Comment on the morphology of the erythrocytes.
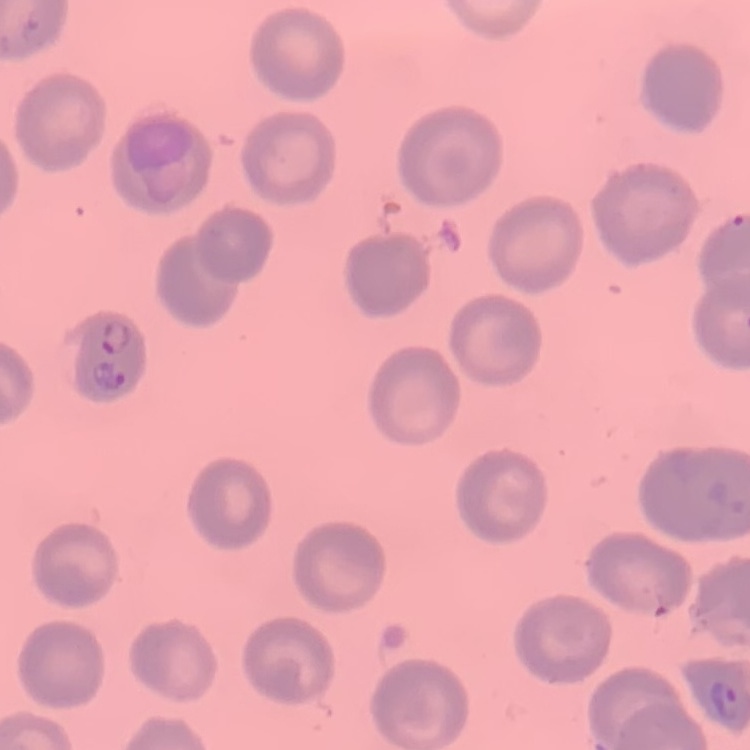
No rouleaux formation.

Stained with either Field's or Giemsa. Thin peripheral smear. One tile cut from a larger photomicrograph.